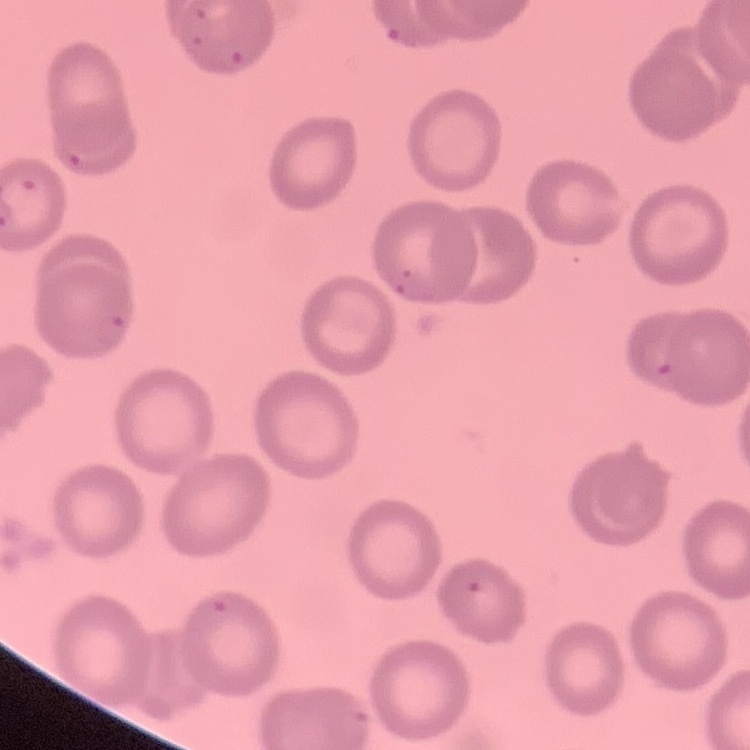
Summary:
  - Red blood cell morphology: no rouleaux formation
  - Stain: Field's or Giemsa
  - Preparation: thin blood smear
  - Image type: square crop of a larger photomicrograph